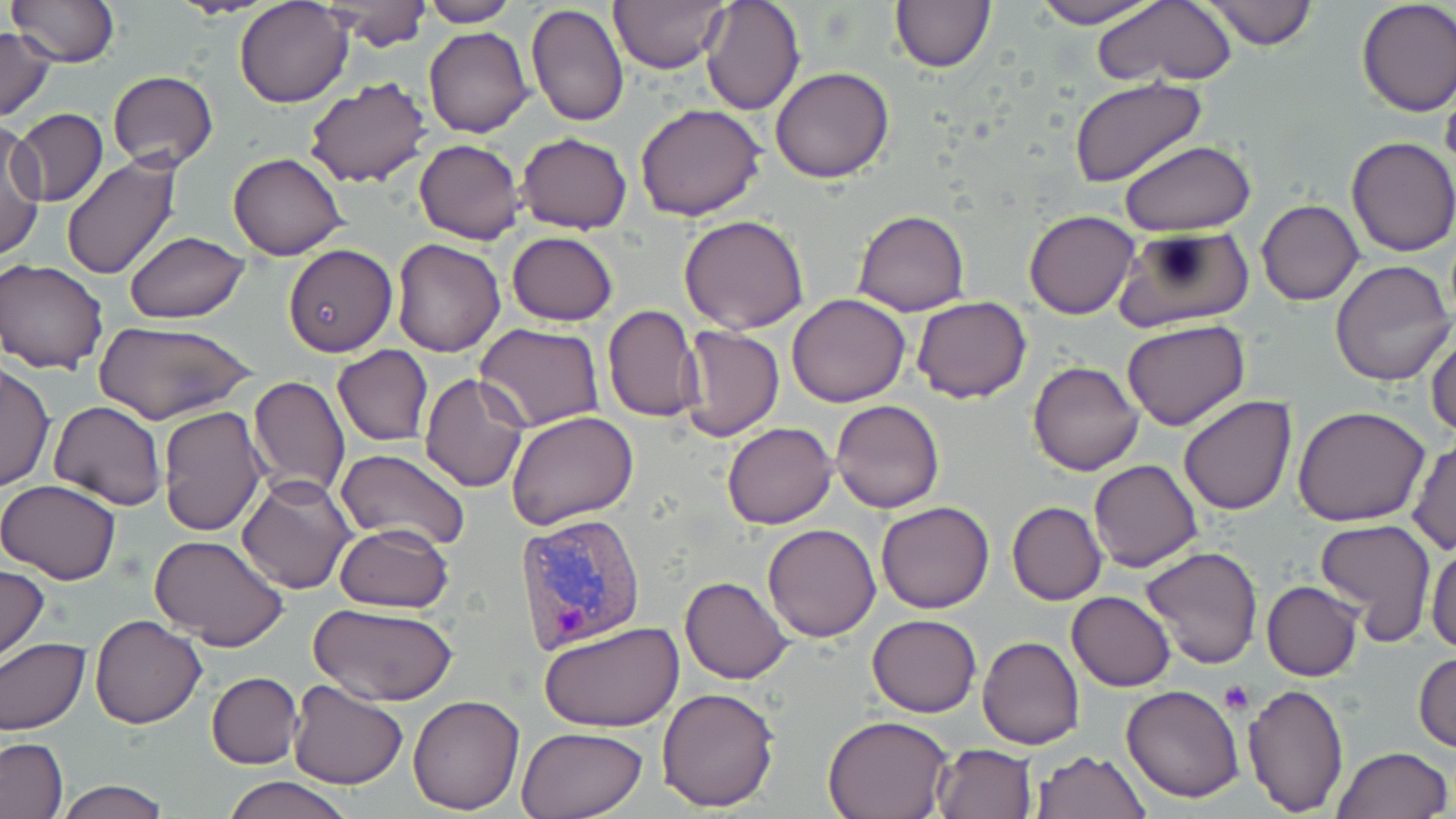

slide-level diagnosis = Plasmodium vivax
image size = 1456×819 pixels
uninfected red blood cell locations = approximate bounding boxes as (x1, y1, x2, y2) in pixels: (8, 0, 121, 68), (235, 0, 352, 107), (607, 0, 728, 73), (700, 0, 804, 116), (1028, 0, 1167, 27), (1090, 0, 1239, 89), (1201, 0, 1318, 49), (1355, 0, 1456, 115), (317, 1, 432, 49), (414, 1, 519, 26), (890, 2, 995, 73), (526, 5, 628, 129), (0, 11, 96, 100), (0, 26, 56, 121), (424, 27, 532, 138), (770, 66, 896, 183), (108, 70, 218, 169), (301, 75, 433, 189), (1067, 75, 1206, 187), (635, 102, 766, 221), (14, 109, 108, 208), (1, 122, 45, 261), (516, 132, 632, 234), (1346, 137, 1456, 256), (414, 139, 525, 245), (1121, 141, 1255, 234), (227, 152, 348, 260), (59, 156, 181, 280), (1257, 199, 1364, 305), (1025, 209, 1139, 319), (852, 210, 969, 316), (679, 214, 808, 333), (1114, 227, 1253, 332), (123, 230, 250, 323), (506, 231, 618, 326), (390, 237, 505, 356), (283, 244, 397, 355), (1, 258, 109, 374), (1330, 260, 1454, 386), (786, 293, 910, 407), (912, 296, 1032, 403), (602, 305, 703, 422), (94, 320, 257, 426), (1121, 320, 1250, 428), (475, 324, 604, 432), (680, 324, 785, 443), (1427, 330, 1456, 438), (331, 345, 434, 447), (1028, 360, 1144, 476), (1, 361, 54, 492), (420, 373, 530, 493), (247, 376, 350, 501), (1178, 396, 1295, 515), (830, 399, 944, 513), (49, 401, 166, 511), (156, 406, 268, 536), (1293, 406, 1430, 527), (507, 410, 639, 530), (722, 422, 837, 529), (1407, 439, 1455, 555), (335, 448, 471, 550), (1087, 460, 1203, 571), (237, 475, 356, 594), (0, 478, 123, 585), (876, 501, 994, 613), (1007, 501, 1107, 604), (1315, 518, 1437, 643), (334, 523, 454, 613), (762, 523, 882, 642), (148, 534, 290, 649), (1426, 539, 1456, 655), (1142, 546, 1263, 669), (0, 565, 49, 662), (681, 576, 792, 684), (1261, 581, 1362, 681), (1067, 591, 1176, 691), (309, 604, 456, 707), (91, 613, 206, 728), (867, 614, 981, 717), (538, 621, 683, 733), (977, 636, 1084, 749), (0, 638, 91, 736), (1412, 652, 1456, 753), (206, 671, 303, 768), (286, 680, 407, 790), (1241, 681, 1351, 815), (1121, 684, 1246, 802), (656, 686, 782, 813), (408, 693, 526, 812), (824, 716, 952, 819), (516, 726, 648, 818), (0, 738, 67, 819), (931, 743, 1036, 819), (1331, 745, 1453, 819), (1030, 751, 1148, 818), (222, 777, 354, 819), (57, 780, 169, 818)
stain = May-Grünwald-Giemsa
platelet locations = approximate bounding boxes as (x1, y1, x2, y2) in pixels: (1219, 681, 1252, 712)
preparation = thin blood smear
modality = light microscopy
Plasmodium vivax-infected red blood cell locations = approximate bounding boxes as (x1, y1, x2, y2) in pixels: (513, 512, 648, 656)
field of view = single
magnification = 1000x